Name the parasite shown.
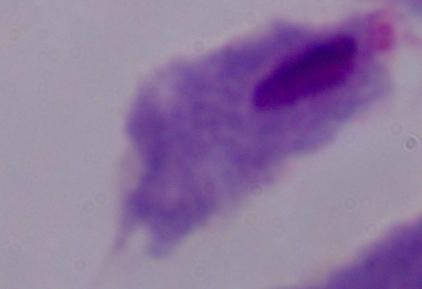
This is a trichomonad.

Micrograph. 1000x magnification.